Give the extent of all uninfected red blood cells.
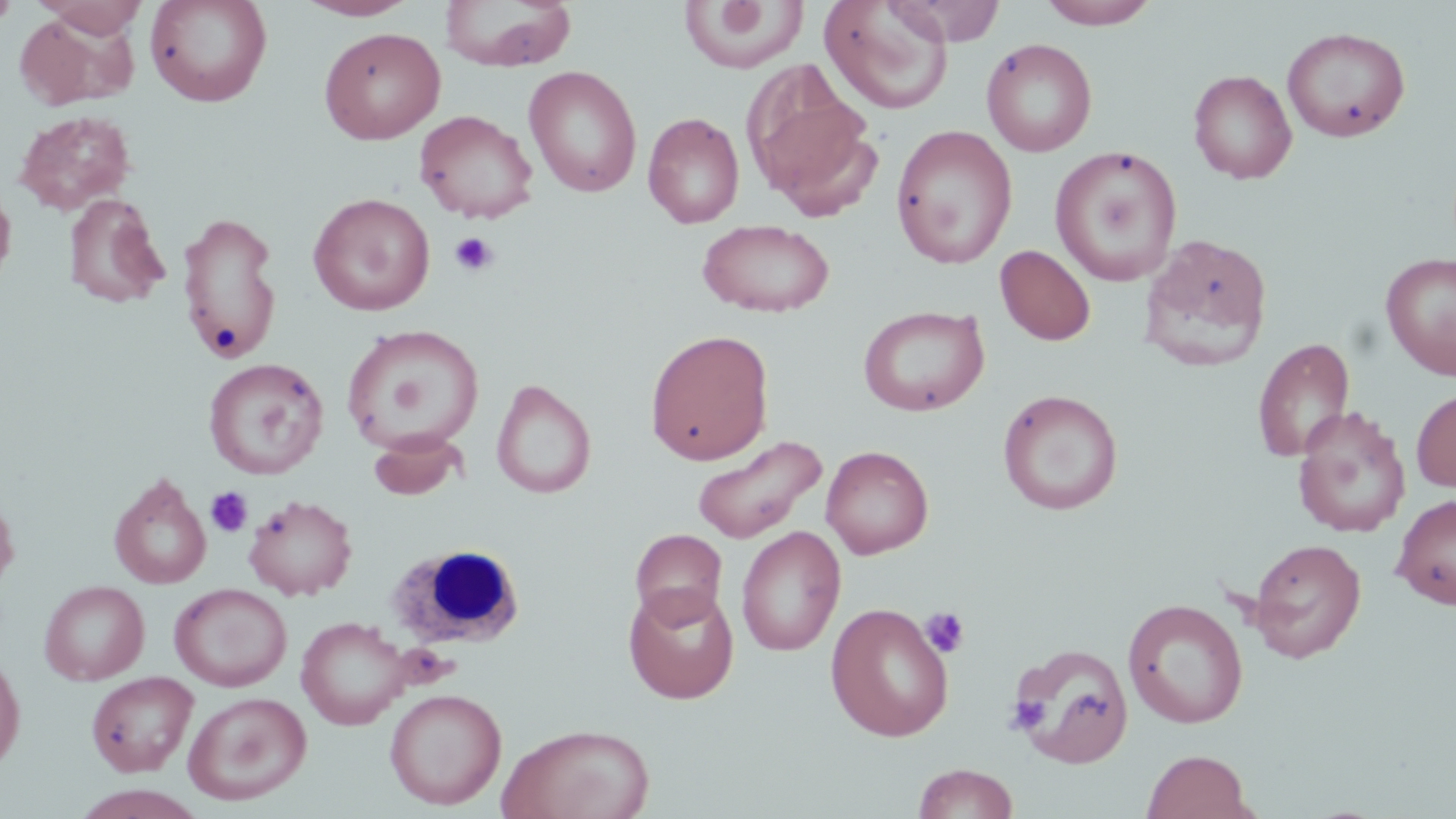

Approximate bounding boxes as (x1, y1, x2, y2) in pixels.
Uninfected red blood cells: (0, 0, 18, 29), (33, 0, 150, 38), (144, 0, 273, 108), (294, 0, 419, 21), (440, 0, 578, 72), (885, 0, 1007, 46), (1037, 0, 1161, 28), (677, 1, 808, 74), (819, 1, 955, 114), (13, 11, 137, 111), (319, 26, 445, 144), (1282, 26, 1411, 143), (982, 38, 1098, 157), (741, 62, 881, 216), (523, 66, 642, 198), (1188, 69, 1297, 183), (415, 109, 538, 224), (14, 110, 136, 215), (643, 111, 746, 229), (891, 124, 1018, 269), (1050, 145, 1183, 287), (0, 183, 16, 291), (308, 192, 435, 316), (63, 193, 170, 309), (176, 211, 283, 365), (697, 218, 834, 318), (1138, 233, 1274, 372), (995, 245, 1096, 346), (1380, 252, 1456, 379), (858, 305, 990, 416), (341, 323, 484, 455), (644, 329, 774, 466), (1252, 338, 1355, 462), (203, 358, 329, 481), (491, 379, 596, 499), (1412, 386, 1456, 493), (998, 389, 1123, 514), (1292, 407, 1412, 538), (370, 428, 468, 501), (692, 434, 827, 545), (821, 445, 934, 559), (108, 472, 212, 590), (0, 490, 20, 597), (1392, 493, 1456, 610), (244, 494, 358, 600), (736, 526, 846, 656), (629, 527, 728, 628), (1246, 537, 1367, 662), (39, 580, 150, 685), (170, 583, 292, 691), (624, 585, 739, 703), (1123, 599, 1249, 729), (826, 602, 954, 742), (296, 617, 410, 730), (1011, 643, 1134, 769), (0, 648, 26, 773), (85, 671, 198, 777), (385, 688, 507, 810), (184, 691, 312, 806), (498, 723, 656, 819), (1141, 749, 1256, 819), (912, 763, 1019, 819), (70, 785, 209, 819).

slide_level_diagnosis: no evidence of blood parasites
modality: light microscopy
white_blood_cell_locations: 'approximate bounding boxes as (x1, y1, x2, y2) in pixels: (387, 543, 526, 649)'
image_size: 1456×819 pixels
stain: May-Grünwald-Giemsa
field_of_view: single
platelet_locations: 'approximate bounding boxes as (x1, y1, x2, y2) in pixels: (448, 231, 500, 277), (206, 487, 252, 537), (921, 606, 970, 658), (1007, 695, 1049, 734)'
magnification: 1000x
preparation: thin blood film